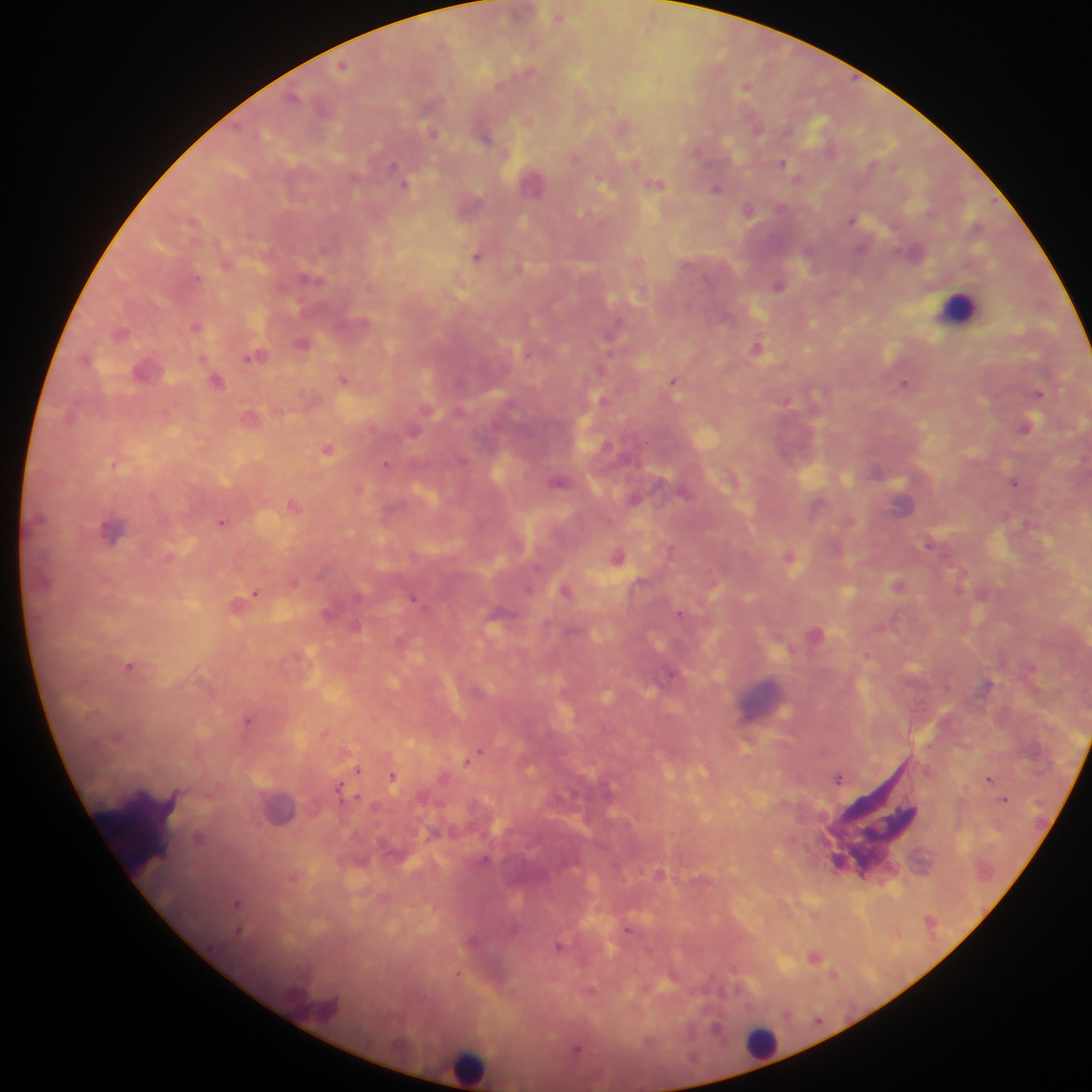
capture: mobile-phone photograph through a microscope
field_of_view: single
country: Ghana
leukocyte_locations: 'approximate centers as (x, y) in pixels: (957, 306), (763, 703), (279, 807), (763, 1040), (470, 1066)'
image_size: 1092×1092 pixels
preparation: thick blood film
object_labeled_both_malaria_parasite_and_leukocyte_by_the_source: 'approximate centers as (x, y) in pixels: (112, 531)'
malaria_parasite_locations: 'approximate centers as (x, y) in pixels: (560, 16), (343, 65), (746, 87), (293, 97), (758, 129), (432, 132), (485, 137), (576, 158), (783, 162), (394, 167), (354, 177), (535, 184), (656, 184), (405, 185), (716, 188), (780, 207), (749, 210), (194, 220), (854, 220), (860, 249), (477, 256), (197, 277), (309, 278), (779, 285), (195, 327), (610, 336), (302, 343), (757, 347), (255, 356), (599, 370), (344, 379), (217, 380), (674, 381), (904, 382), (1039, 393), (251, 416), (1027, 426), (413, 432), (328, 449), (463, 460), (386, 463), (559, 481), (1015, 483), (633, 499), (294, 505), (221, 522), (929, 543), (618, 556), (790, 556), (897, 585), (529, 589), (565, 590), (254, 593), (414, 598), (680, 613), (356, 626), (129, 667), (669, 675), (247, 719), (478, 752), (358, 770), (393, 777), (839, 777), (989, 779), (340, 789), (1005, 799), (199, 838), (485, 859), (238, 904), (628, 930), (239, 931), (559, 946), (814, 957), (458, 973), (577, 1049)'